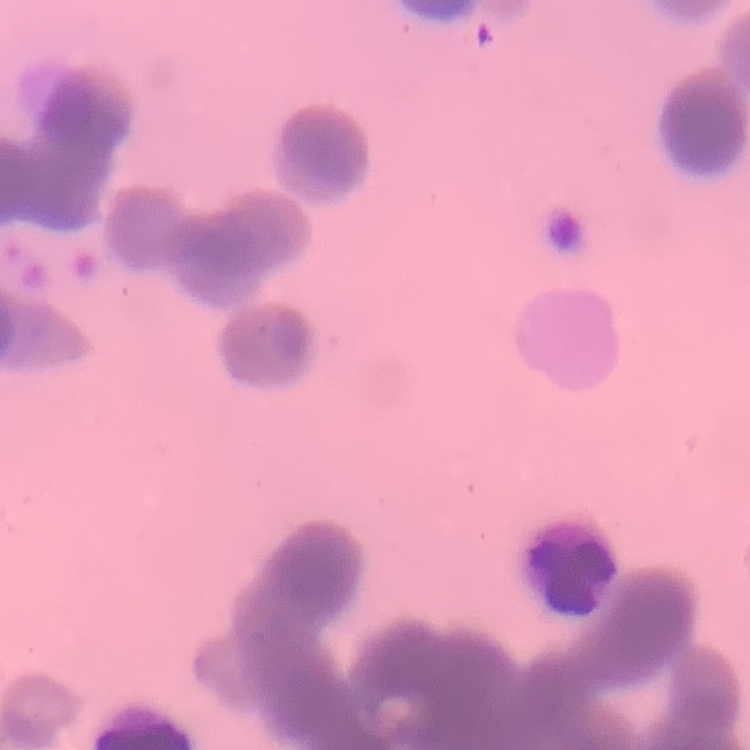 The red blood cells show rouleaux formation. One tile cut from a larger photomicrograph. Thin blood film. Stained with either Field's or Giemsa.